Assess this cell for malaria.
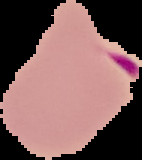

It is parasitized.

Image is 142×160 pixels. From a thin blood film. The area outside the segmented cell region is set to black.